Draw a bounding box around every parasitised red blood cell.
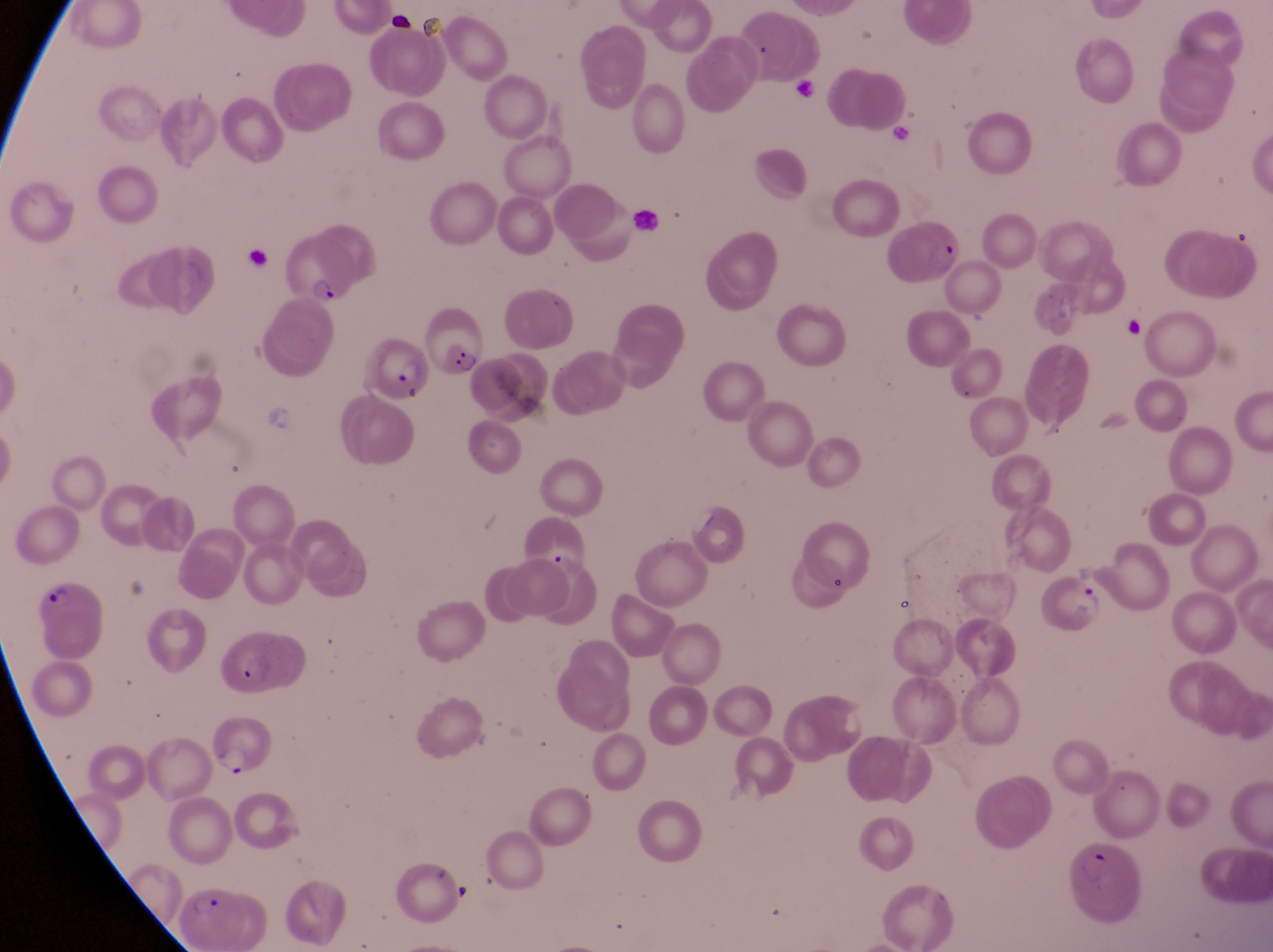

Approximate bounding boxes as {left, top, right, bottom} in pixels.
Parasitised red blood cells: {894, 209, 966, 287}, {278, 230, 356, 310}, {367, 325, 429, 405}, {1043, 569, 1106, 639}, {32, 580, 107, 657}, {218, 637, 305, 699}, {199, 714, 277, 781}, {1064, 841, 1144, 926}, {177, 882, 237, 947}.

Summary:
  - Trophozoite locations: {440, 332, 482, 379}
  - Field of view: single
  - Preparation: thin blood smear
  - Magnification: 1000x
  - Country: Uganda
  - Capture: smartphone photograph through the eyepiece of an Olympus CX-23 microscope
  - Image size: 1273×952 pixels